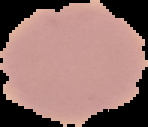
Summary:
  - Image size: 148×127 pixels
  - Image type: segmented cell region on a black background
  - Preparation: thin blood film
  - Result: no Plasmodium parasites seen